Comment on the morphology of the red blood cells.
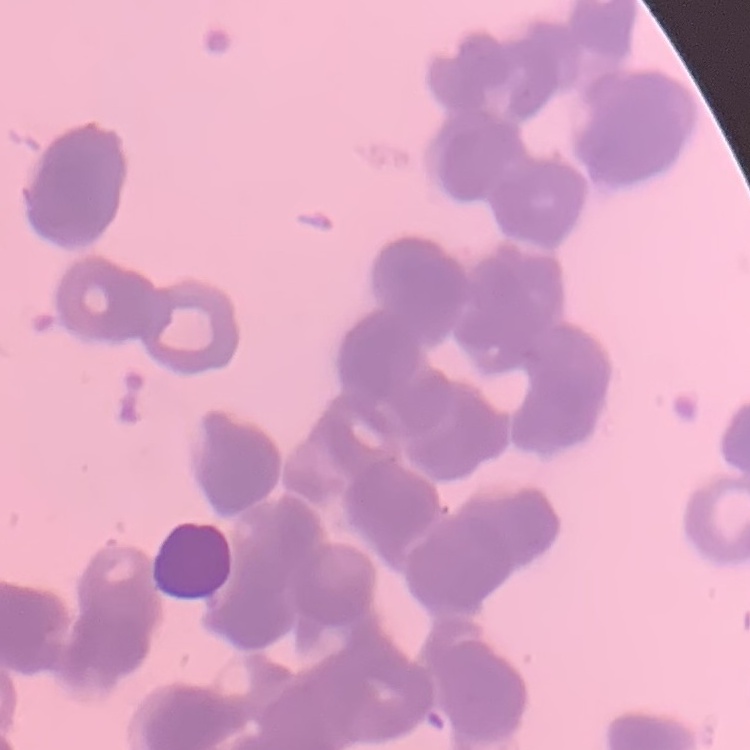

Rouleaux formation.

image type = square crop of a larger photomicrograph
preparation = thin peripheral smear
stain = Field's or Giemsa